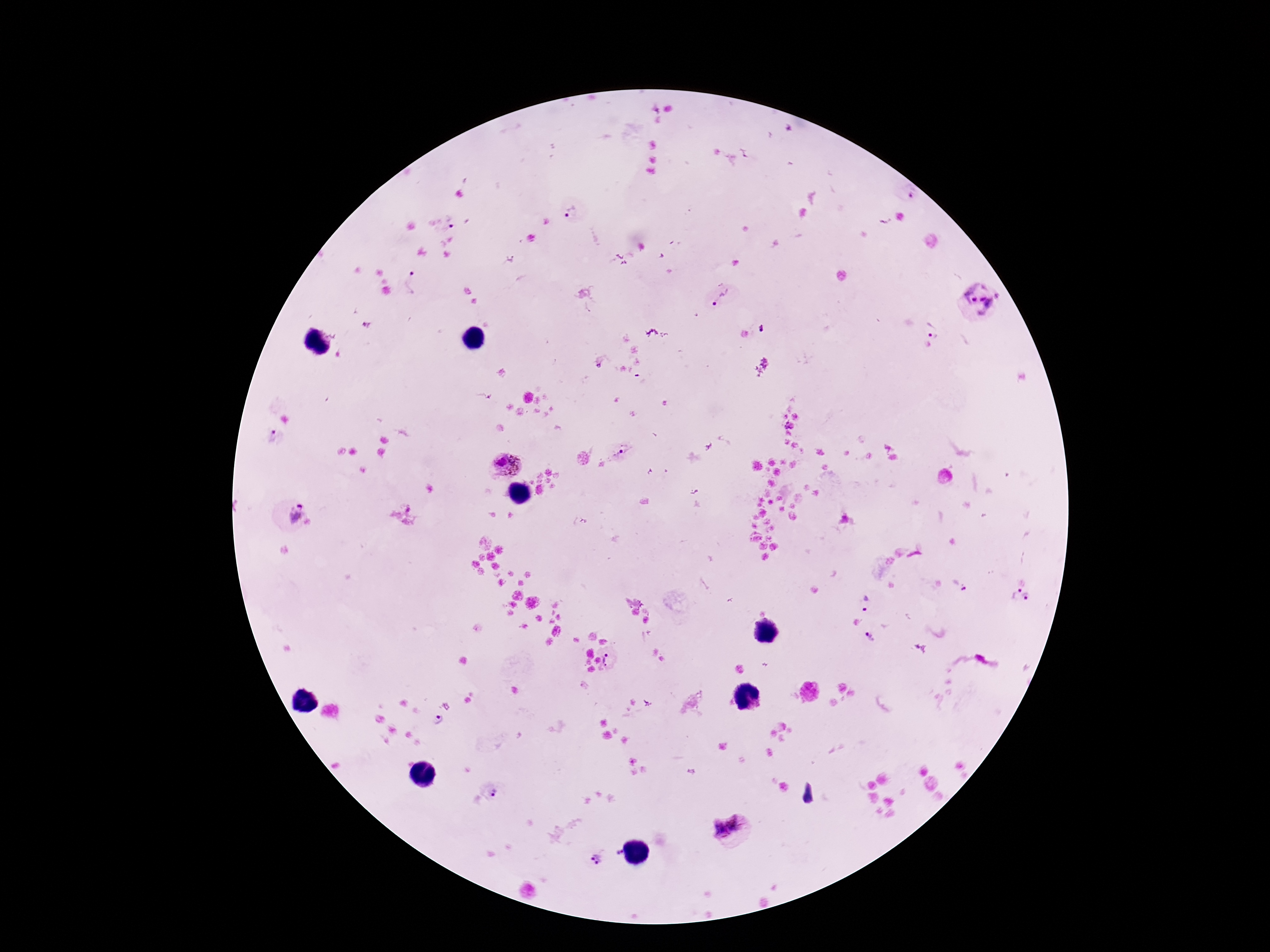 Approximate centers as {x, y} in pixels. Plasmodium parasite locations: {909, 191}, {566, 211}, {448, 224}, {509, 260}, {414, 282}, {981, 296}, {720, 298}, {932, 329}, {762, 330}, {276, 438}, {626, 450}, {506, 464}, {295, 512}, {960, 584}, {1013, 594}, {1028, 598}, {865, 603}, {869, 638}, {612, 657}, {438, 719}, {495, 790}, {738, 821}, {717, 828}, {619, 852}, {595, 859}. Giemsa-stained preparation. Thick blood film. Image is 1270×952 pixels. One field from this slide. 100x magnification. Patient malaria status: positive. Photographed through the microscope eyepiece with a smartphone camera.